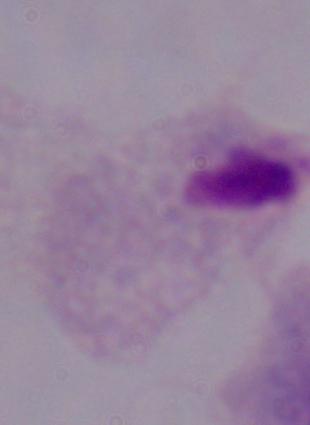
Summary:
  - Identification: trichomonad
  - Magnification: 1000x
  - Modality: micrograph